Assess the morphology of the erythrocytes.
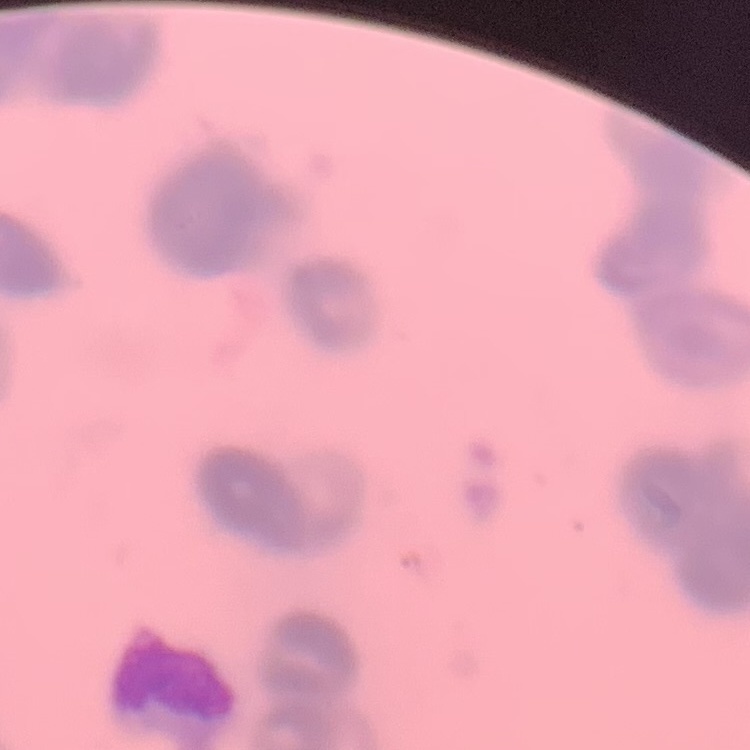

Rouleaux formation.

{
  "stain": "Field's or Giemsa",
  "preparation": "thin blood film",
  "image_type": "one tile cut from a larger photomicrograph"
}